Name the parasite shown.
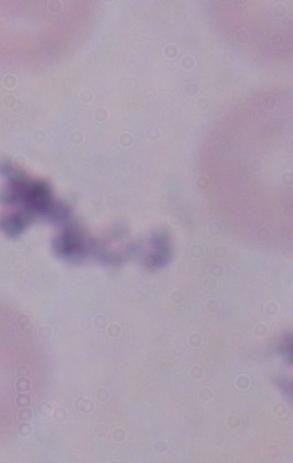

This is a trypanosome.

Summary:
  - Magnification: 1000x
  - Modality: photomicrograph